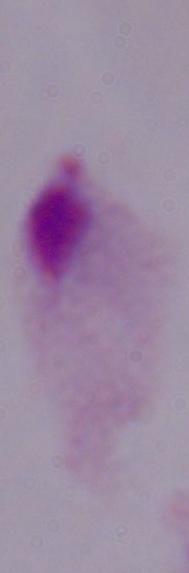

Captured at 1000x magnification. A trichomonad is seen. Micrograph.